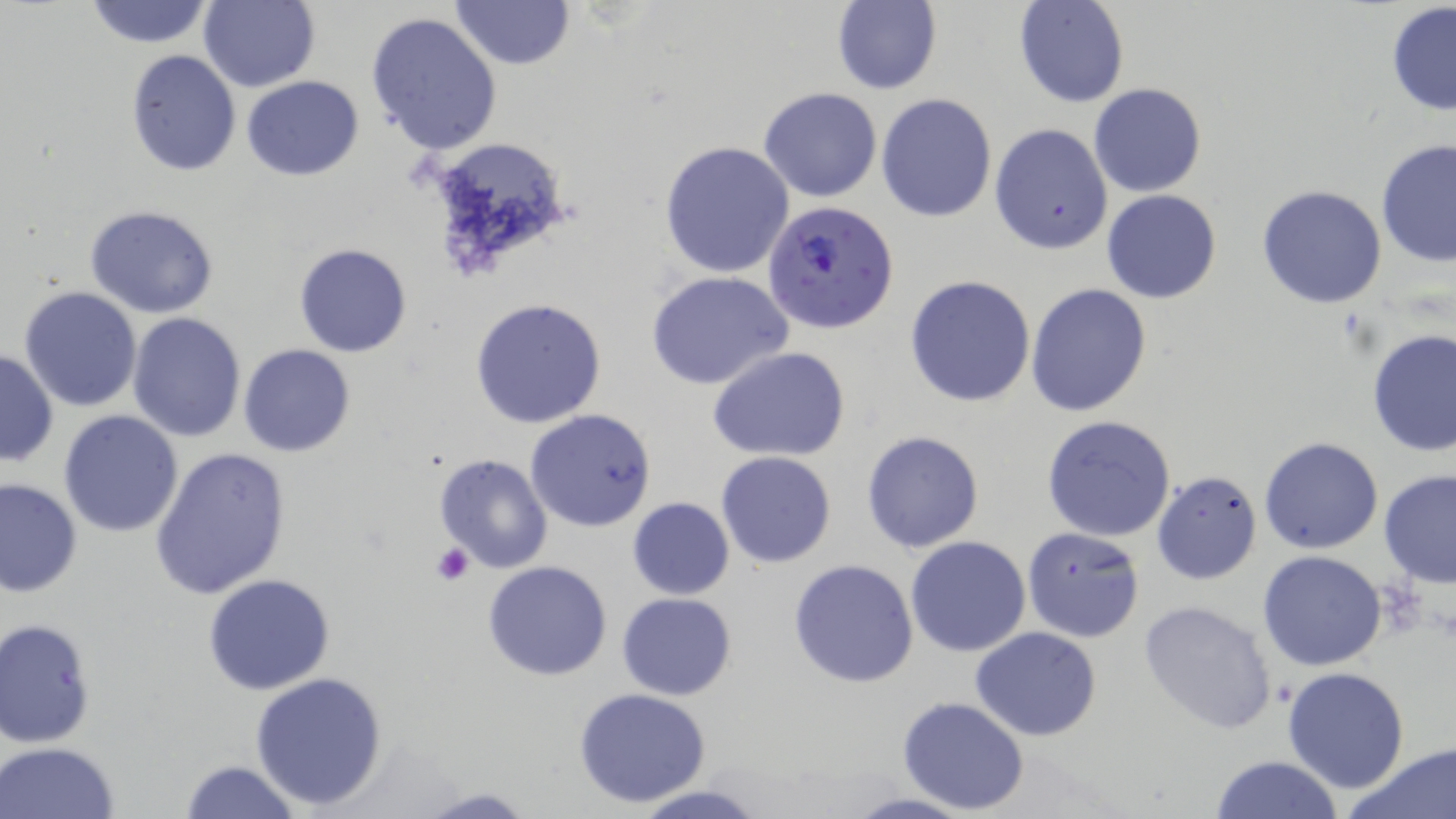 Approximate bounding boxes as [x1, y1, x2, y2] in pixels. Platelet locations: [431, 544, 473, 586]. Uninfected red blood cell locations: [82, 0, 214, 48], [198, 0, 319, 91], [451, 0, 575, 70], [1013, 0, 1129, 108], [832, 1, 941, 94], [1385, 3, 1456, 116], [367, 12, 502, 154], [125, 49, 241, 176], [241, 75, 365, 180], [1088, 84, 1209, 198], [758, 87, 883, 203], [876, 93, 997, 222], [989, 123, 1113, 254], [423, 135, 576, 267], [1376, 138, 1455, 270], [658, 141, 795, 279], [1257, 185, 1387, 308], [1100, 190, 1222, 304], [83, 204, 222, 317], [293, 242, 412, 357], [647, 271, 793, 391], [905, 275, 1037, 408], [1025, 283, 1151, 417], [19, 285, 143, 413], [469, 297, 608, 428], [128, 313, 246, 442], [1367, 328, 1455, 458], [238, 343, 357, 457], [0, 347, 58, 467], [708, 348, 850, 461], [59, 409, 184, 538], [525, 409, 657, 532], [1042, 414, 1177, 541], [860, 429, 985, 553], [1259, 437, 1384, 554], [149, 446, 293, 601], [716, 451, 836, 567], [433, 452, 557, 574], [1152, 470, 1261, 584], [1377, 470, 1456, 590], [0, 478, 81, 596], [626, 497, 735, 599], [1021, 526, 1145, 642], [905, 536, 1032, 657], [1258, 551, 1388, 672], [788, 558, 920, 688], [482, 560, 613, 681], [203, 573, 336, 696], [617, 592, 736, 701], [1137, 599, 1281, 737], [0, 617, 97, 748], [972, 626, 1102, 741], [1281, 667, 1411, 795], [247, 672, 389, 811], [573, 689, 714, 807], [898, 696, 1030, 815], [2, 741, 122, 818], [1353, 742, 1456, 819], [1209, 754, 1344, 819], [176, 758, 302, 819], [625, 783, 772, 819], [412, 786, 538, 818], [838, 792, 978, 819]. Plasmodium falciparum-infected red blood cell locations: [764, 199, 899, 337]. Slide-level diagnosis: Plasmodium falciparum. Thin blood smear. 1000x magnification. May-Grünwald-Giemsa-stained preparation. Optical microscopy. Single field of view. Image is 1456×819 pixels.